Comment on the morphology of the erythrocytes.
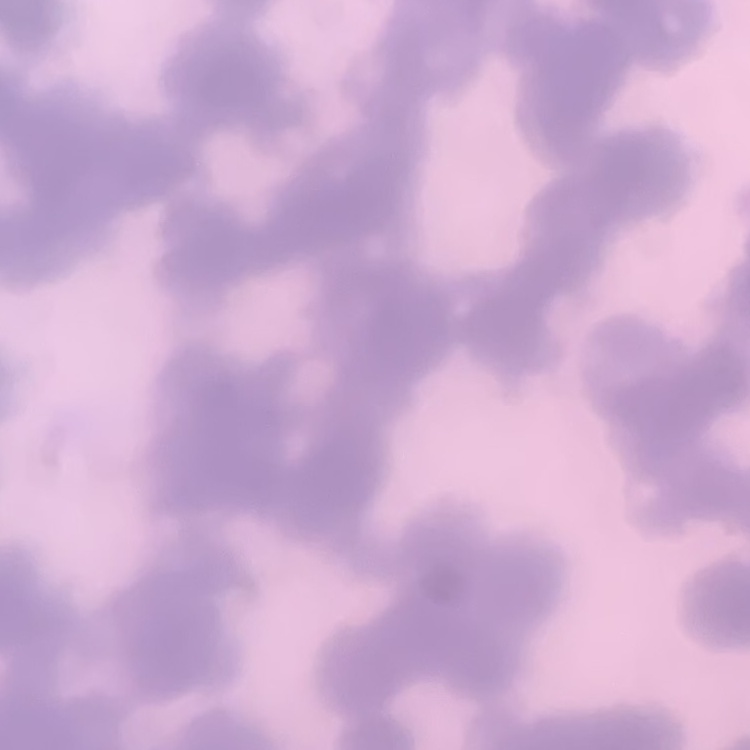
They show rouleaux formation.

preparation = thin blood film
image type = square crop of a larger photomicrograph
stain = Field's or Giemsa